Report the malaria status of this cell.
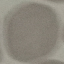

Uninfected.

Giemsa stain. Automatically extracted cell patch, resized to 64 × 64 pixels. Acquired by smartphone through the microscope eyepiece. Thin blood smear.